Report the malaria status of this cell.
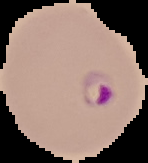

Parasitized.

Image is 148×163 pixels. Segmented cell region on a black background. From a thin blood film.